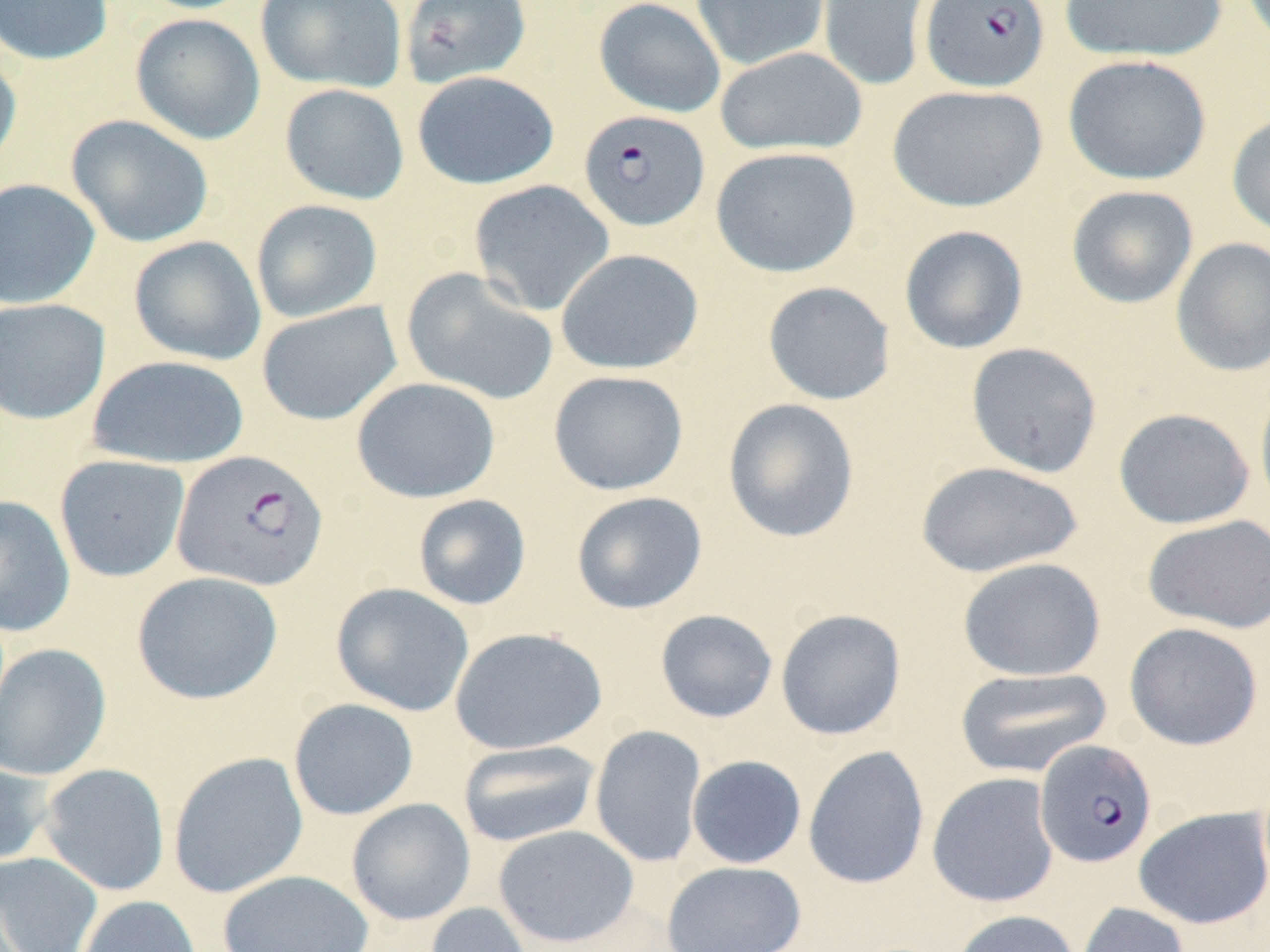 Approximate bounding boxes as [x1, y1, x2, y2] in pixels. Uninfected red blood cell locations: [0, 0, 114, 66], [130, 0, 261, 14], [255, 0, 406, 93], [399, 0, 532, 88], [593, 0, 726, 117], [691, 0, 830, 71], [816, 0, 933, 93], [1060, 0, 1228, 63], [130, 13, 266, 144], [714, 46, 867, 156], [0, 49, 22, 174], [1063, 54, 1212, 185], [411, 70, 559, 190], [279, 83, 409, 205], [887, 83, 1049, 212], [1227, 111, 1270, 239], [66, 114, 214, 248], [710, 146, 861, 277], [0, 178, 100, 309], [468, 179, 615, 316], [1066, 185, 1199, 309], [250, 199, 383, 323], [898, 224, 1029, 354], [129, 235, 266, 366], [1170, 236, 1270, 377], [556, 248, 703, 375], [401, 267, 559, 406], [762, 281, 896, 405], [0, 298, 110, 425], [256, 300, 402, 425], [965, 342, 1103, 478], [87, 354, 250, 469], [548, 369, 689, 495], [351, 377, 501, 503], [1254, 378, 1270, 518], [722, 397, 860, 543], [1112, 407, 1255, 529], [54, 454, 190, 582], [915, 460, 1084, 578], [571, 491, 707, 614], [0, 494, 76, 637], [413, 494, 531, 610], [1142, 514, 1270, 634], [957, 557, 1106, 682], [131, 571, 283, 705], [331, 582, 474, 716], [775, 608, 907, 740], [655, 609, 778, 723], [1124, 621, 1264, 750], [449, 626, 607, 755], [0, 642, 112, 781], [954, 666, 1113, 779], [288, 698, 419, 820], [589, 724, 707, 868], [457, 740, 602, 847], [803, 746, 930, 890], [168, 751, 309, 899], [686, 755, 807, 869], [0, 759, 53, 867], [39, 762, 170, 896], [927, 772, 1060, 908], [346, 798, 476, 925], [1133, 806, 1270, 929], [493, 824, 639, 948], [0, 851, 103, 952], [661, 861, 806, 952], [217, 870, 374, 952], [76, 895, 203, 952], [1074, 901, 1190, 952], [423, 902, 534, 952], [950, 909, 1080, 952]. Plasmodium falciparum-infected red blood cell locations: [919, 0, 1050, 93], [578, 109, 710, 232], [172, 450, 329, 592], [1034, 739, 1158, 868]. Slide-level diagnosis: Plasmodium falciparum. Light microscopy. Image is 1270×952 pixels. One field of a larger specimen. Thin blood smear. 1000x magnification. May-Grünwald-Giemsa stain.